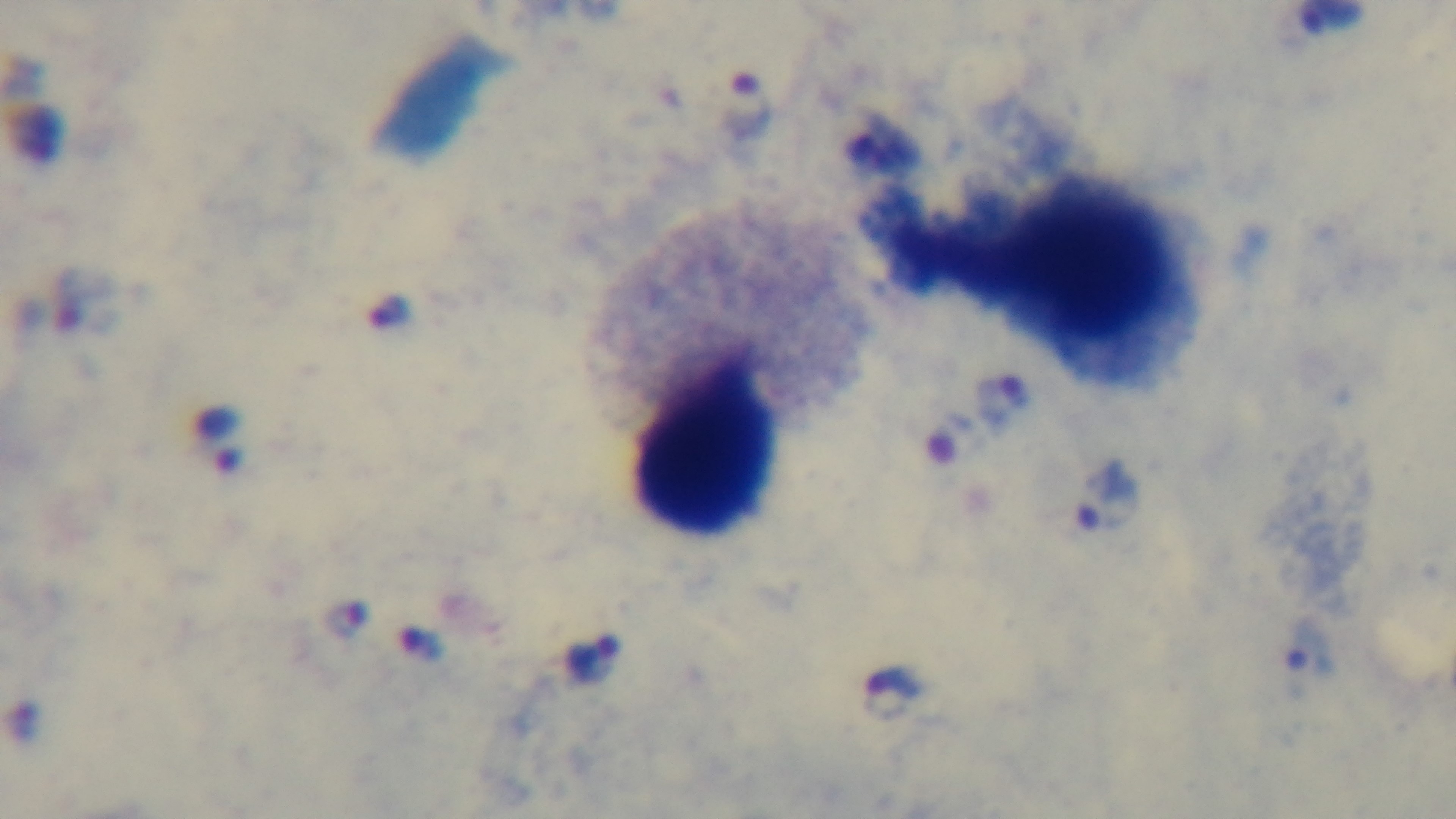
100x oil-immersion objective. Malaria status: positive. One field from the slide. Preparation: thick blood film. Light microscopy. Giemsa stain. Captured with a mounted 4K digital camera.